Outline each blood parasite and name the species.
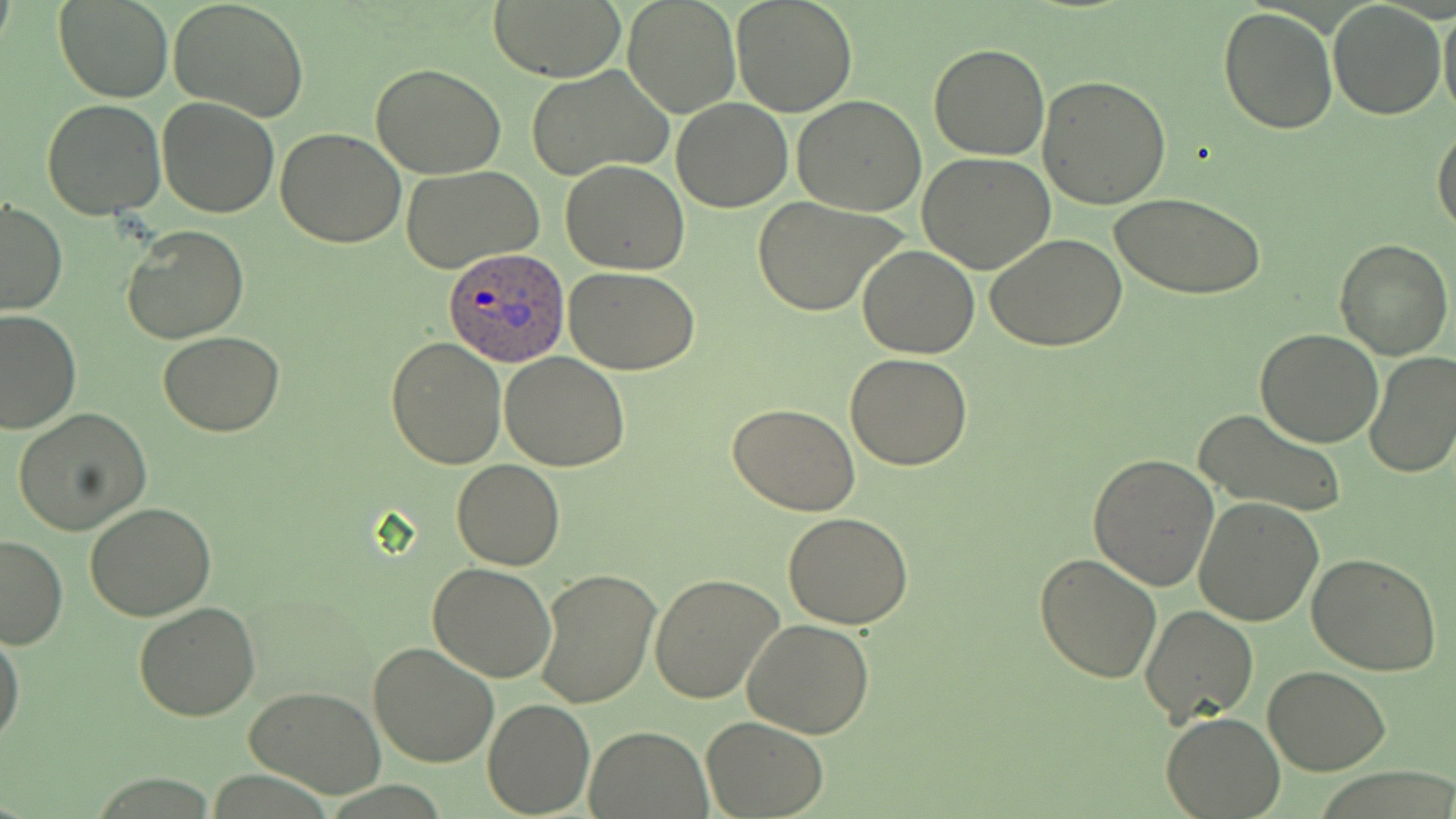
Approximate bounding boxes as (x1, y1, x2, y2) in pixels.
Plasmodium ovale-infected red blood cells: (442, 250, 570, 367).
No Plasmodium falciparum, Plasmodium malariae, Plasmodium vivax, Babesia divergens, or Trypanosoma brucei observed.

Uninfected red blood cell locations: (57, 0, 173, 103), (168, 0, 311, 122), (488, 0, 624, 81), (731, 0, 858, 117), (1329, 1, 1446, 119), (1438, 1, 1456, 122), (623, 2, 737, 116), (1219, 5, 1337, 133), (929, 43, 1050, 160), (371, 62, 506, 178), (525, 65, 671, 181), (1040, 75, 1172, 210), (791, 95, 927, 216), (156, 97, 281, 219), (671, 97, 793, 211), (42, 100, 167, 220), (1432, 125, 1456, 239), (276, 127, 406, 247), (918, 152, 1055, 273), (561, 160, 689, 275), (402, 166, 544, 275), (1111, 192, 1266, 300), (751, 195, 908, 317), (1, 198, 67, 314), (123, 226, 249, 344), (986, 233, 1126, 352), (1333, 236, 1454, 360), (859, 246, 981, 359), (566, 268, 700, 375), (0, 310, 80, 434), (1255, 327, 1384, 446), (158, 331, 286, 436), (386, 337, 506, 468), (499, 351, 630, 471), (1363, 352, 1456, 480), (844, 353, 974, 471), (728, 401, 861, 515), (13, 408, 151, 535), (1194, 410, 1348, 520), (1087, 453, 1220, 593), (451, 459, 564, 570), (1194, 496, 1325, 627), (85, 502, 217, 622), (784, 511, 913, 628), (0, 533, 69, 651), (1035, 552, 1163, 684), (1307, 553, 1442, 677), (428, 562, 557, 682), (534, 565, 661, 709), (649, 573, 785, 703), (132, 602, 260, 720), (1139, 604, 1259, 727), (742, 617, 875, 737), (0, 627, 23, 747), (367, 641, 499, 770), (1264, 665, 1390, 776), (244, 686, 387, 798), (483, 698, 595, 817), (1161, 712, 1286, 818), (702, 716, 828, 818), (585, 726, 711, 817). Slide-level diagnosis: Plasmodium ovale. Captured at 1000x magnification. May-Grünwald-Giemsa-stained preparation. Image is 1456×819 pixels. Thin blood film. Optical microscopy. One field of a larger specimen.